State which parasite is depicted.
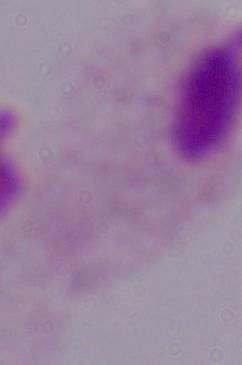
A trichomonad.

magnification = 1000x
modality = micrograph